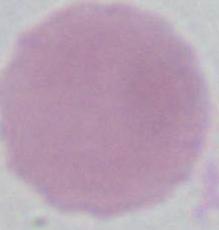
magnification = 1000x
modality = micrograph
identification = red blood cell